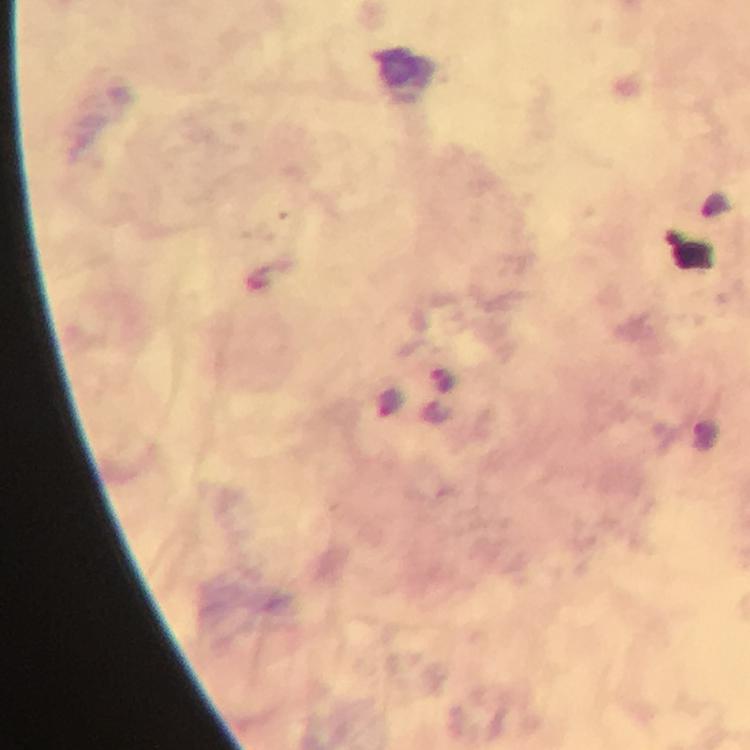 Approximate object centers, in pixels from the top-left corner. Plasmodium parasite locations: (x=441, y=380), (x=389, y=404). Immersion oil was used. Image is 750×750 pixels. Giemsa-stained preparation. A crop from one field of view. Thick smear. 100x magnification. From a diagnostic examination for malaria. Photographed through the microscope with a smartphone camera.